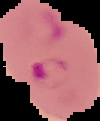
Summary:
  - Result: Plasmodium parasites detected
  - Image size: 100×121 pixels
  - Preparation: thin blood smear
  - Image type: segmented cell region on a black background